Name the parasite shown.
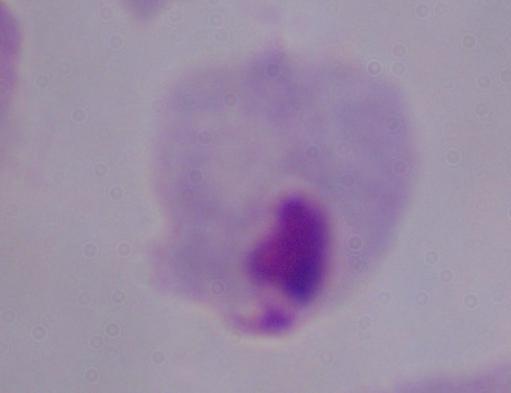
A trichomonad.

Photomicrograph. Captured at 1000x magnification.